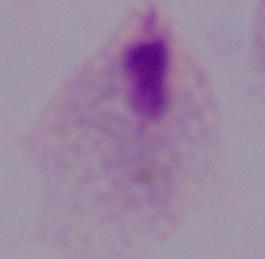

A trichomonad is shown. 1000x magnification. Micrograph.